State which parasite is depicted.
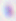
Toxoplasma gondii.

{
  "magnification": "400x",
  "modality": "photomicrograph"
}